State which parasite is depicted.
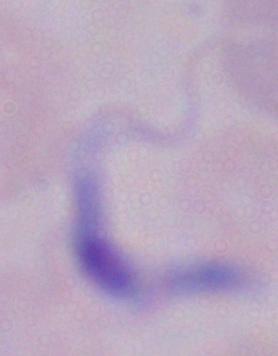

A trypanosome.

magnification = 1000x
modality = micrograph